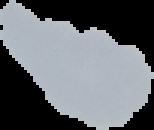

From a thin blood film. The area outside the segmented cell region is set to black. Malaria status: uninfected. Image is 154×130 pixels.